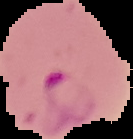

image size = 133×139 pixels
image type = segmented cell region on a black background
preparation = thin blood film
malaria status = parasitized